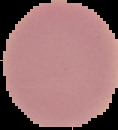
Summary:
  - Image type: segmented cell region on a black background
  - Result: no Plasmodium parasites seen
  - Image size: 118×130 pixels
  - Preparation: thin blood smear